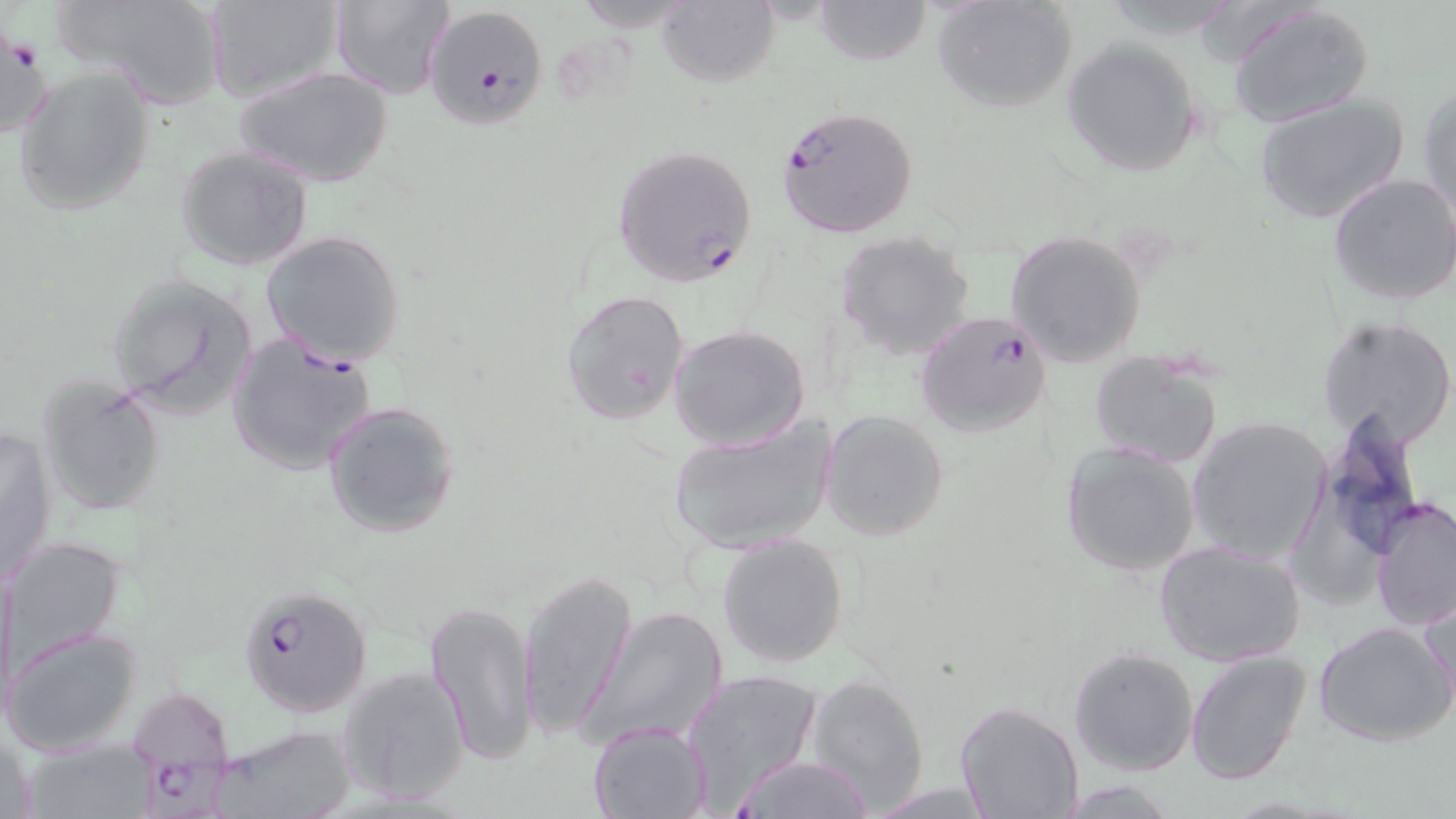

Approximate bounding boxes as (x1, y1, x2, y2) in pixels. Plasmodium falciparum-infected red blood cell locations: (422, 3, 551, 132), (776, 105, 920, 238), (610, 144, 759, 289), (915, 309, 1057, 440), (225, 330, 378, 476), (239, 585, 371, 717), (127, 685, 242, 808). Uninfected red blood cell locations: (56, 0, 227, 109), (207, 0, 343, 105), (329, 0, 454, 99), (656, 0, 778, 88), (814, 0, 931, 65), (932, 1, 1077, 114), (1227, 3, 1375, 127), (0, 23, 50, 144), (1060, 36, 1204, 178), (11, 64, 155, 218), (235, 66, 393, 188), (1419, 81, 1455, 222), (1253, 94, 1410, 224), (174, 145, 314, 270), (1327, 172, 1456, 307), (1004, 230, 1147, 369), (833, 232, 977, 360), (259, 233, 406, 372), (105, 271, 260, 418), (560, 289, 692, 427), (1317, 314, 1456, 451), (669, 323, 810, 450), (1089, 348, 1226, 470), (35, 373, 168, 520), (322, 399, 461, 539), (819, 409, 949, 540), (1316, 414, 1429, 566), (1186, 415, 1334, 565), (666, 416, 836, 554), (1, 424, 58, 585), (1059, 441, 1203, 576), (1369, 497, 1454, 634), (718, 533, 849, 668), (5, 537, 125, 664), (1154, 538, 1306, 667), (0, 559, 17, 718), (518, 570, 636, 741), (1419, 588, 1455, 720), (424, 600, 540, 767), (581, 605, 731, 748), (1314, 622, 1454, 747), (3, 624, 143, 757), (1069, 647, 1200, 775), (1186, 650, 1311, 785), (335, 664, 471, 807), (681, 668, 824, 805), (804, 674, 930, 809), (954, 701, 1085, 819), (587, 720, 712, 818), (215, 724, 357, 819), (22, 740, 157, 817), (727, 753, 876, 819). Slide-level diagnosis: Plasmodium falciparum. One field of a larger specimen. May-Grünwald-Giemsa-stained preparation. Image is 1456×819 pixels. 1000x magnification. Optical microscopy. Thin blood film.